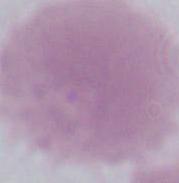

Summary:
  - Modality: micrograph
  - Magnification: 1000x
  - Identification: erythrocyte